Assess this cell for malaria.
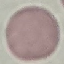
It is uninfected.

Summary:
  - Capture: smartphone through the microscope eyepiece
  - Image type: automatically extracted cell patch, resized to 64 × 64 pixels
  - Stain: Giemsa
  - Preparation: thin blood smear